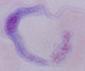

Summary:
  - Identification: trypanosome
  - Modality: micrograph
  - Magnification: 1000x